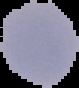

{
  "image_size": "79×88 pixels",
  "malaria_status": "uninfected",
  "image_type": "segmented cell region with the area outside set to black",
  "preparation": "thin blood film"
}